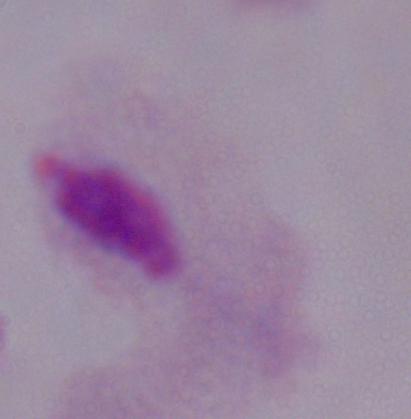
Captured at 1000x magnification. Photomicrograph. A trichomonad is seen.